Report the malaria status of this cell.
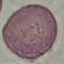

It is uninfected.

Giemsa stain. Acquired by smartphone through the microscope eyepiece. Cell patch, automatically extracted from a larger field of view and resized to 64 × 64 pixels. Thin smear of blood.